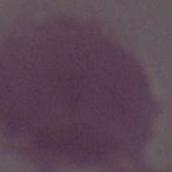

magnification = 1000x
modality = photomicrograph
identification = erythrocyte